Name the blood parasite species.
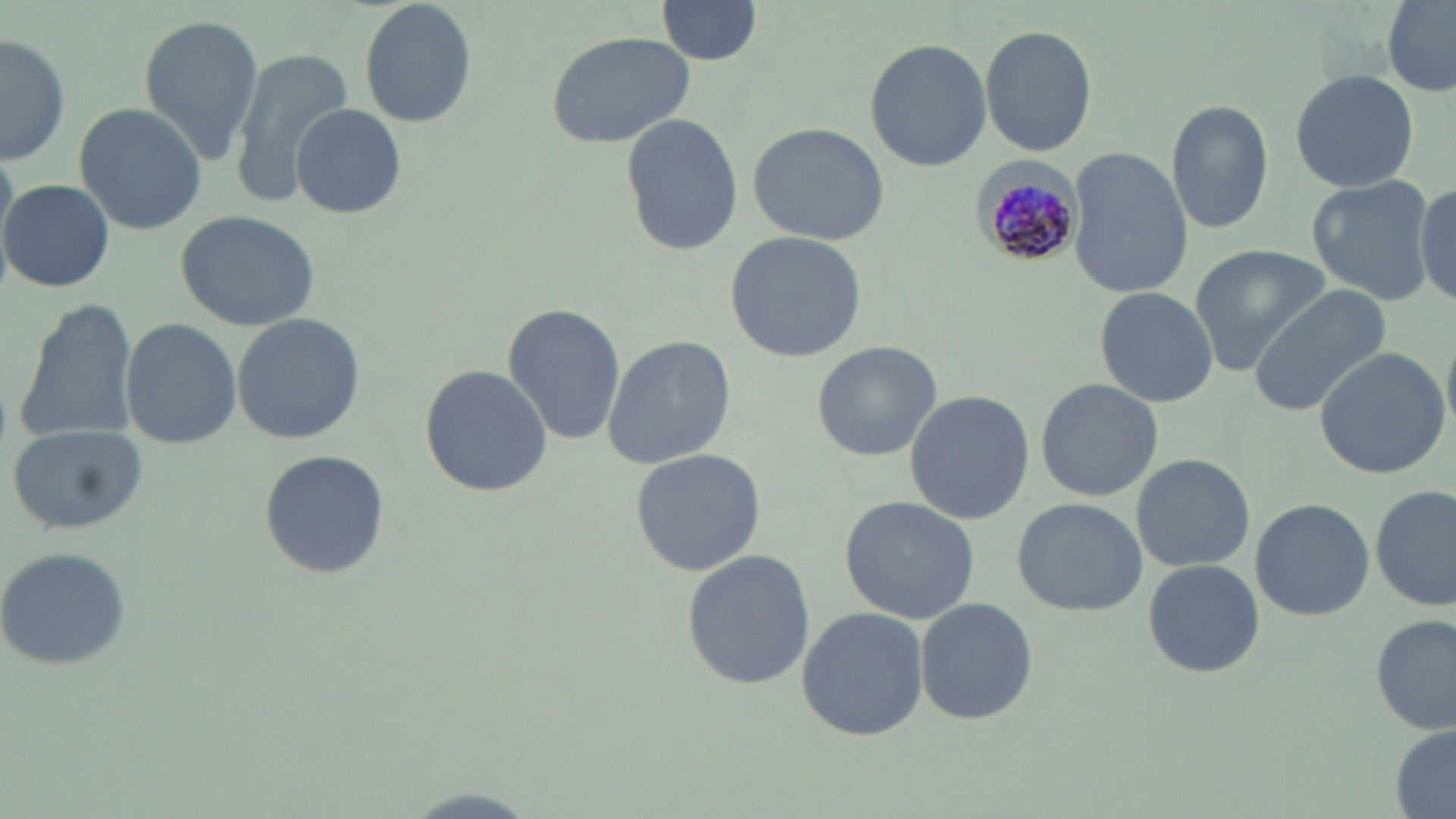
Plasmodium malariae.

image size = 1456×819 pixels
modality = light microscopy
preparation = thin blood film
Plasmodium malariae-infected red blood cell locations = approximate bounding boxes as [x1, y1, x2, y2] in pixels: [973, 154, 1083, 270]
uninfected red blood cell locations = approximate bounding boxes as [x1, y1, x2, y2] in pixels: [359, 0, 476, 127], [656, 0, 763, 67], [1379, 4, 1456, 96], [137, 13, 263, 160], [980, 23, 1099, 158], [546, 30, 697, 148], [1, 31, 70, 167], [864, 36, 992, 174], [227, 47, 352, 200], [1288, 67, 1420, 194], [75, 102, 205, 233], [1167, 102, 1274, 233], [292, 104, 407, 219], [620, 112, 741, 256], [746, 121, 890, 245], [1067, 149, 1192, 298], [1308, 176, 1434, 304], [3, 178, 114, 293], [1413, 178, 1455, 308], [174, 207, 322, 332], [725, 229, 868, 362], [1189, 245, 1329, 371], [1248, 283, 1391, 417], [1096, 287, 1215, 406], [14, 299, 140, 447], [503, 303, 625, 444], [232, 314, 364, 443], [120, 316, 242, 450], [240, 324, 377, 554], [602, 333, 735, 470], [811, 341, 942, 462], [1312, 345, 1451, 480], [420, 364, 552, 498], [1035, 378, 1164, 501], [906, 392, 1033, 522], [6, 422, 147, 534], [629, 448, 766, 576], [258, 451, 389, 578], [1130, 452, 1255, 572], [1372, 485, 1454, 612], [840, 495, 980, 625], [1012, 497, 1146, 615], [1250, 497, 1374, 620], [0, 546, 134, 670], [680, 549, 815, 690], [1142, 558, 1264, 679], [915, 598, 1037, 725], [797, 606, 928, 742], [1372, 616, 1455, 735], [1387, 724, 1456, 816], [395, 786, 546, 819]
stain = May-Grünwald-Giemsa
field of view = single
magnification = 1000x